Give the position of every leukocyte visible.
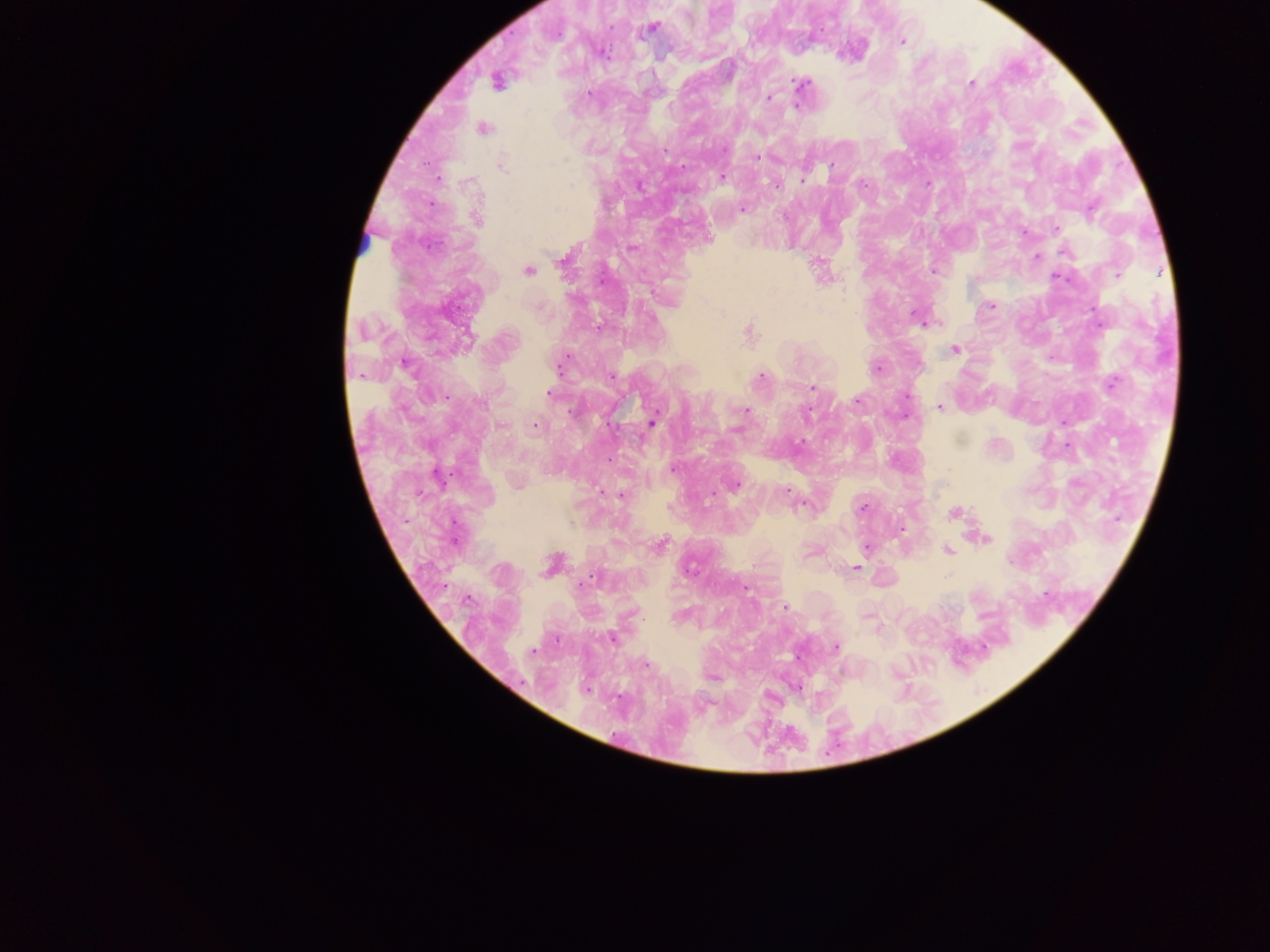
No leukocytes observed.

Approximate centers as {x, y} in pixels.
Summary:
  - Malaria parasite locations: {651, 28}, {901, 41}, {601, 53}, {497, 81}, {801, 84}, {972, 84}, {590, 91}, {768, 97}, {796, 106}, {483, 129}, {757, 156}, {500, 164}, {723, 176}, {802, 179}, {861, 184}, {927, 184}, {742, 209}, {476, 219}, {1056, 229}, {1024, 232}, {631, 248}, {1037, 256}, {565, 259}, {528, 270}, {933, 271}, {1117, 274}, {990, 305}, {921, 319}, {598, 327}, {748, 332}, {955, 350}, {405, 363}, {560, 363}, {876, 368}, {611, 375}, {760, 376}, {1110, 383}, {812, 388}, {549, 393}, {857, 400}, {939, 406}, {746, 410}, {905, 415}, {653, 422}, {535, 426}, {673, 469}, {517, 482}, {733, 484}, {787, 490}, {621, 495}, {803, 503}, {862, 508}, {953, 513}, {901, 527}, {984, 538}, {659, 544}, {866, 548}, {947, 550}, {811, 552}, {552, 564}, {855, 567}, {785, 607}, {866, 616}, {612, 637}, {835, 647}, {644, 663}, {713, 678}, {796, 686}, {585, 689}
  - Preparation: thick blood smear
  - Field of view: single
  - Country: Ghana
  - Image size: 1270×952 pixels
  - Capture: mobile-phone photograph through a microscope